Comment on the morphology of the red blood cells.
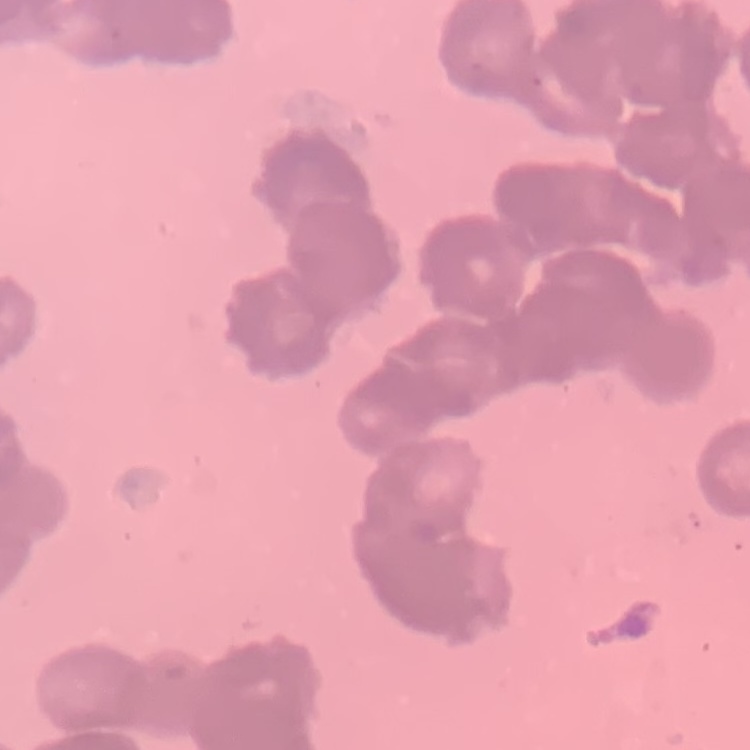

They show rouleaux formation.

Field's or Giemsa stain. One tile cut from a larger photomicrograph. Thin blood film.